State the blood parasite species.
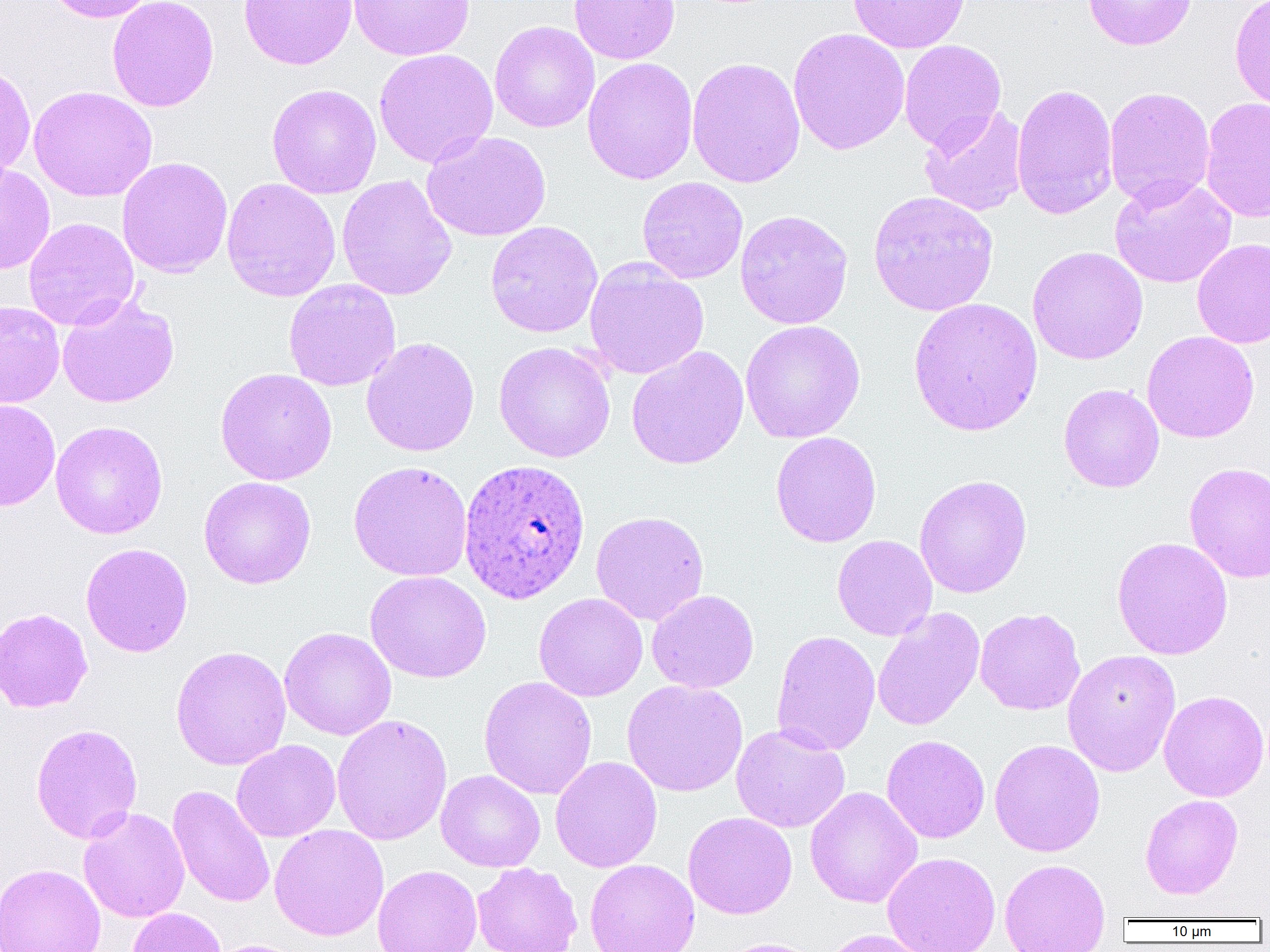
Plasmodium ovale.

Summary:
  - Coordinate format: approximate bounding boxes as (x1, y1, x2, y2) in pixels
  - Uninfected red blood cell locations: (43, 0, 158, 23), (107, 0, 219, 112), (239, 0, 357, 70), (348, 0, 475, 61), (569, 0, 680, 64), (848, 0, 971, 53), (1082, 0, 1197, 50), (1230, 0, 1270, 111), (489, 20, 600, 133), (788, 27, 910, 156), (899, 40, 1007, 154), (374, 49, 498, 167), (686, 56, 806, 188), (582, 57, 698, 185), (0, 62, 36, 182), (266, 83, 382, 199), (1011, 83, 1118, 220), (28, 86, 158, 202), (1104, 86, 1216, 208), (1200, 97, 1270, 223), (919, 105, 1028, 217), (422, 131, 551, 242), (116, 156, 233, 278), (0, 163, 56, 274), (337, 175, 457, 301), (1109, 176, 1237, 289), (221, 177, 341, 302), (637, 177, 748, 284), (867, 190, 999, 317), (735, 209, 853, 329), (23, 217, 139, 331), (485, 221, 603, 338), (1192, 238, 1270, 349), (1027, 246, 1148, 365), (584, 259, 710, 380), (283, 279, 401, 391), (57, 294, 179, 408), (908, 297, 1043, 436), (0, 301, 65, 408), (740, 319, 866, 444), (1141, 331, 1260, 443), (361, 336, 480, 457), (493, 341, 616, 463), (626, 345, 749, 470), (215, 367, 337, 485), (1058, 383, 1164, 493), (0, 399, 60, 511), (50, 421, 168, 539), (770, 431, 882, 548), (348, 460, 473, 582), (1184, 461, 1270, 583), (801, 473, 913, 580), (913, 474, 1032, 599), (198, 476, 316, 589), (590, 510, 709, 626), (832, 535, 937, 641), (1112, 536, 1233, 660), (81, 542, 193, 657), (365, 570, 491, 683), (646, 590, 759, 693), (534, 592, 648, 702), (0, 607, 92, 713), (872, 607, 985, 732), (975, 608, 1086, 715), (279, 627, 396, 740), (771, 630, 881, 756), (170, 645, 291, 771), (1062, 649, 1181, 777), (478, 675, 598, 800), (622, 680, 748, 796), (1159, 690, 1269, 801), (331, 713, 453, 845), (30, 723, 143, 844), (731, 724, 850, 833), (881, 734, 990, 843), (989, 738, 1105, 857), (231, 739, 341, 842), (550, 756, 662, 872), (436, 770, 546, 872), (168, 785, 275, 908), (804, 786, 923, 908), (1140, 794, 1243, 900), (78, 807, 190, 923), (682, 812, 797, 919), (269, 824, 389, 941), (882, 852, 1001, 952), (999, 858, 1110, 952), (585, 859, 699, 952), (472, 862, 582, 952), (0, 863, 105, 952), (372, 864, 483, 952), (126, 907, 226, 952), (819, 929, 938, 952), (714, 937, 823, 952), (206, 939, 310, 952)
  - Plasmodium ovale-infected red blood cell locations: (458, 458, 591, 605)
  - Field of view: single
  - Magnification: 1000x
  - Preparation: thin blood film
  - Image size: 1270×952 pixels
  - Modality: optical microscopy